Give the preparation type.
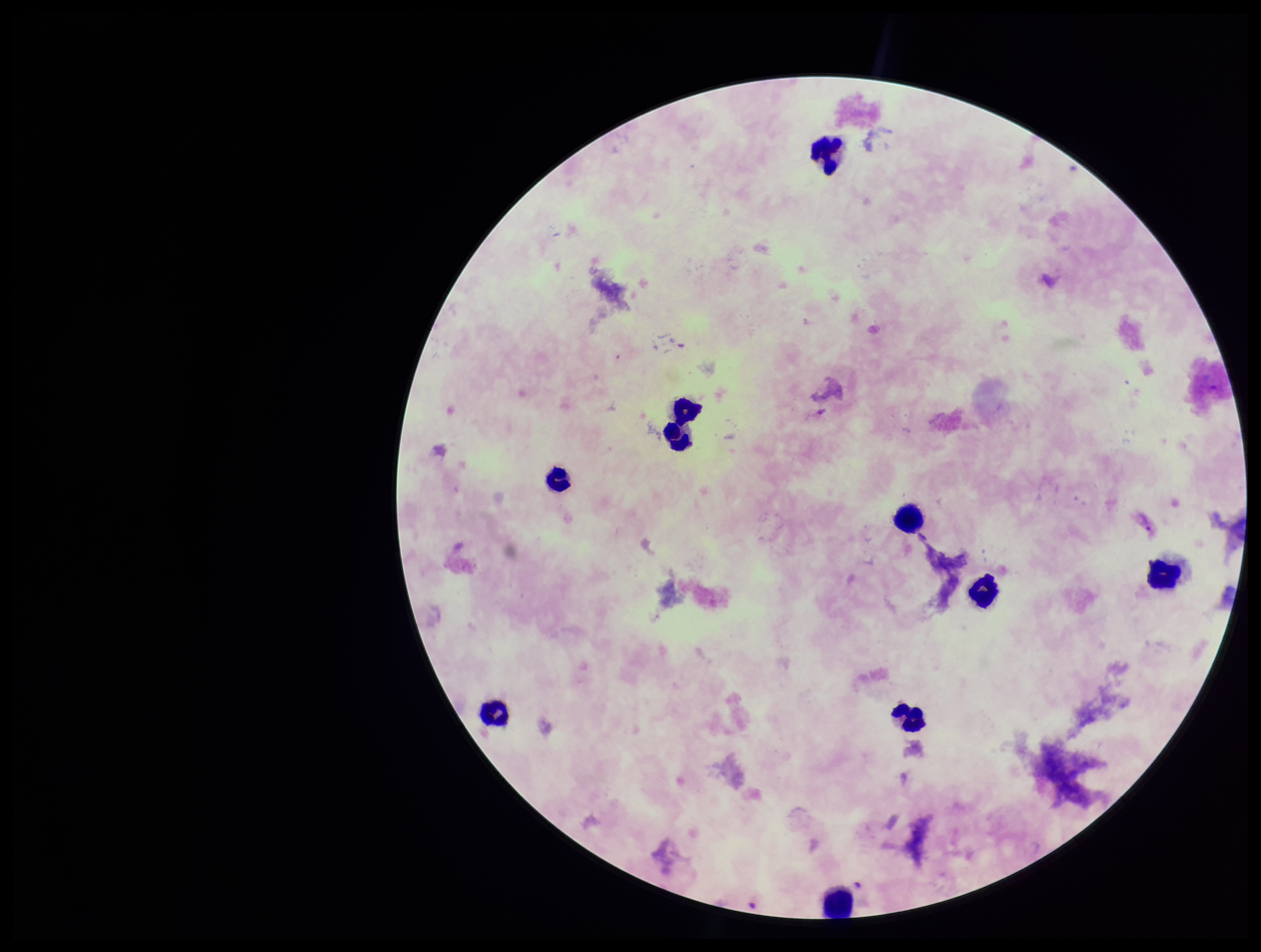
It is a thick blood smear.

Plasmodium parasites = identified
species reported for this patient = Plasmodium vivax
leukocyte count = 10
image size = 1261×952 pixels
parasite count = 1
field of view = one from this slide
capture = smartphone photograph through the microscope eyepiece
patient malaria status = infected
stain = Giemsa